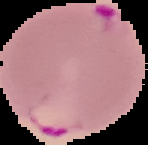
Malaria status: parasitized. From a thin blood film. Cell region segmented out of the field of view; the surrounding area is masked to black. Image is 148×145 pixels.